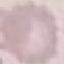
result = no malaria parasites seen
image type = cell patch, automatically extracted from a larger field of view and resized to 64 × 64 pixels
capture = smartphone camera at the microscope eyepiece
preparation = thin blood film
stain = Giemsa